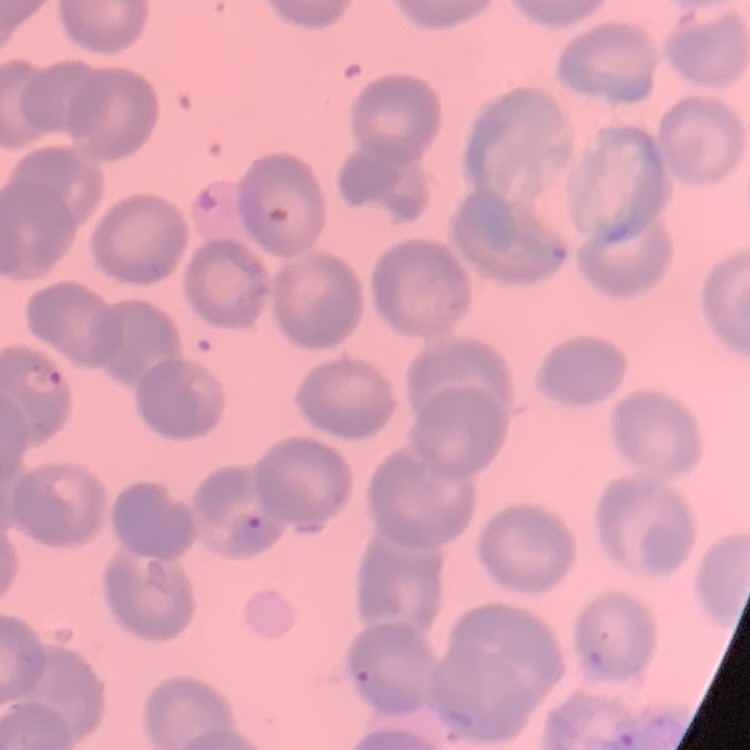
Summary:
  - Erythrocyte morphology: no rouleaux formation
  - Image type: square crop of a larger photomicrograph
  - Preparation: thin blood smear
  - Stain: Field's or Giemsa